Identify the parasite.
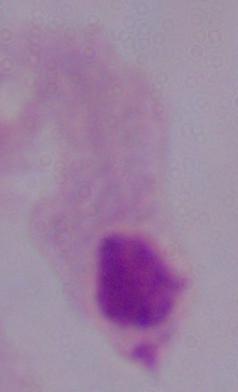

A trichomonad.

Micrograph. Captured at 1000x magnification.